Identify the parasite.
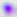
Toxoplasma gondii.

400x magnification. Micrograph.